Outline every Plasmodium parasite.
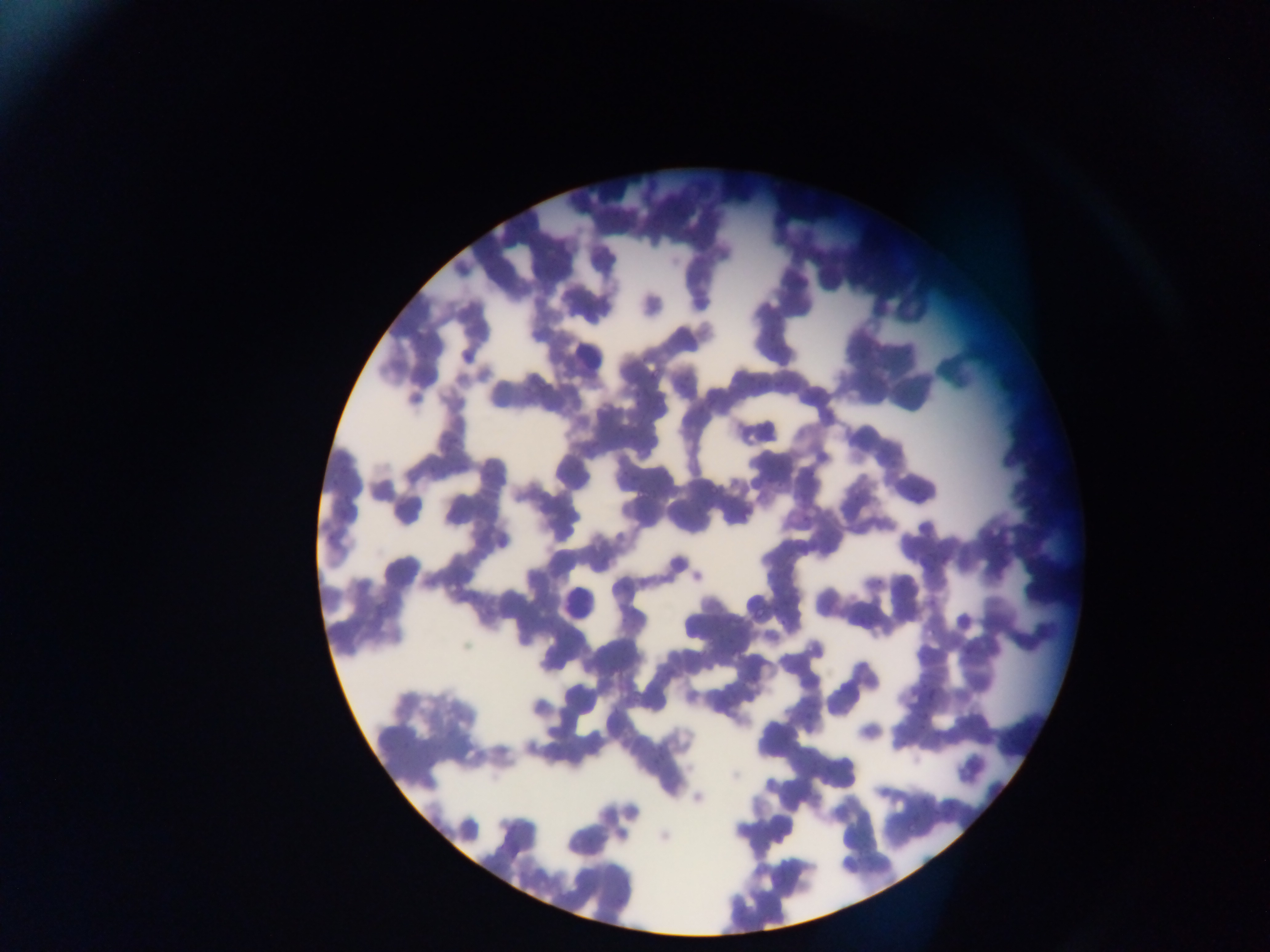
Approximate bounding boxes as left top right bottom in pixels.
Plasmodium parasites: 651 366 662 380; 710 482 721 495; 638 489 651 498; 753 609 767 618; 717 625 732 633; 922 710 931 720; 906 821 921 835.

capture = mobile-phone photograph through a microscope
preparation = thin blood film
country = Ghana
field of view = single
leukocyte locations = approximate bounding boxes as left top right bottom in pixels: 566 336 608 372; 563 584 604 622
image size = 1270×952 pixels